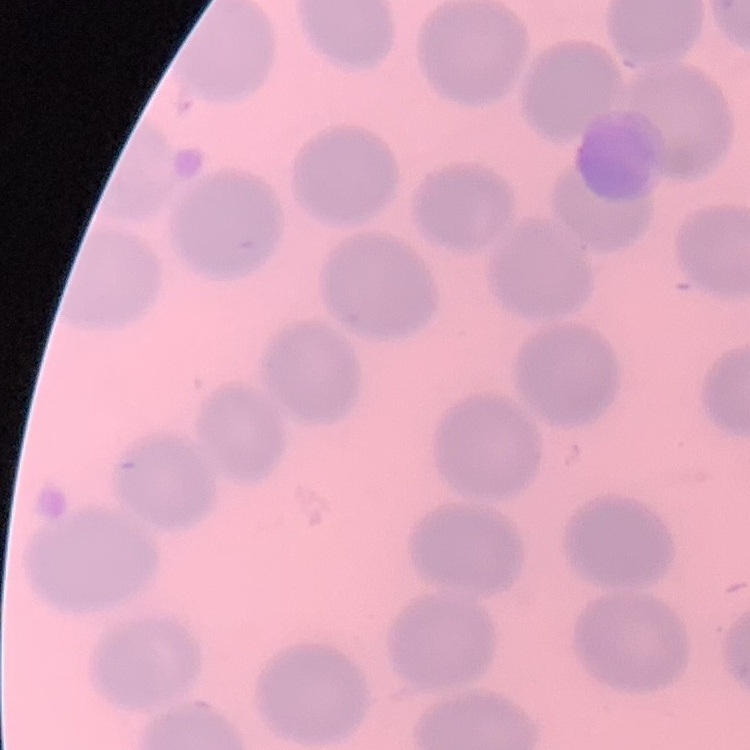

Summary:
  - Erythrocyte morphology: no rouleaux formation
  - Stain: Field's or Giemsa
  - Preparation: thin blood smear
  - Image type: square crop of a larger photomicrograph